Give the position of every leukocyte visible.
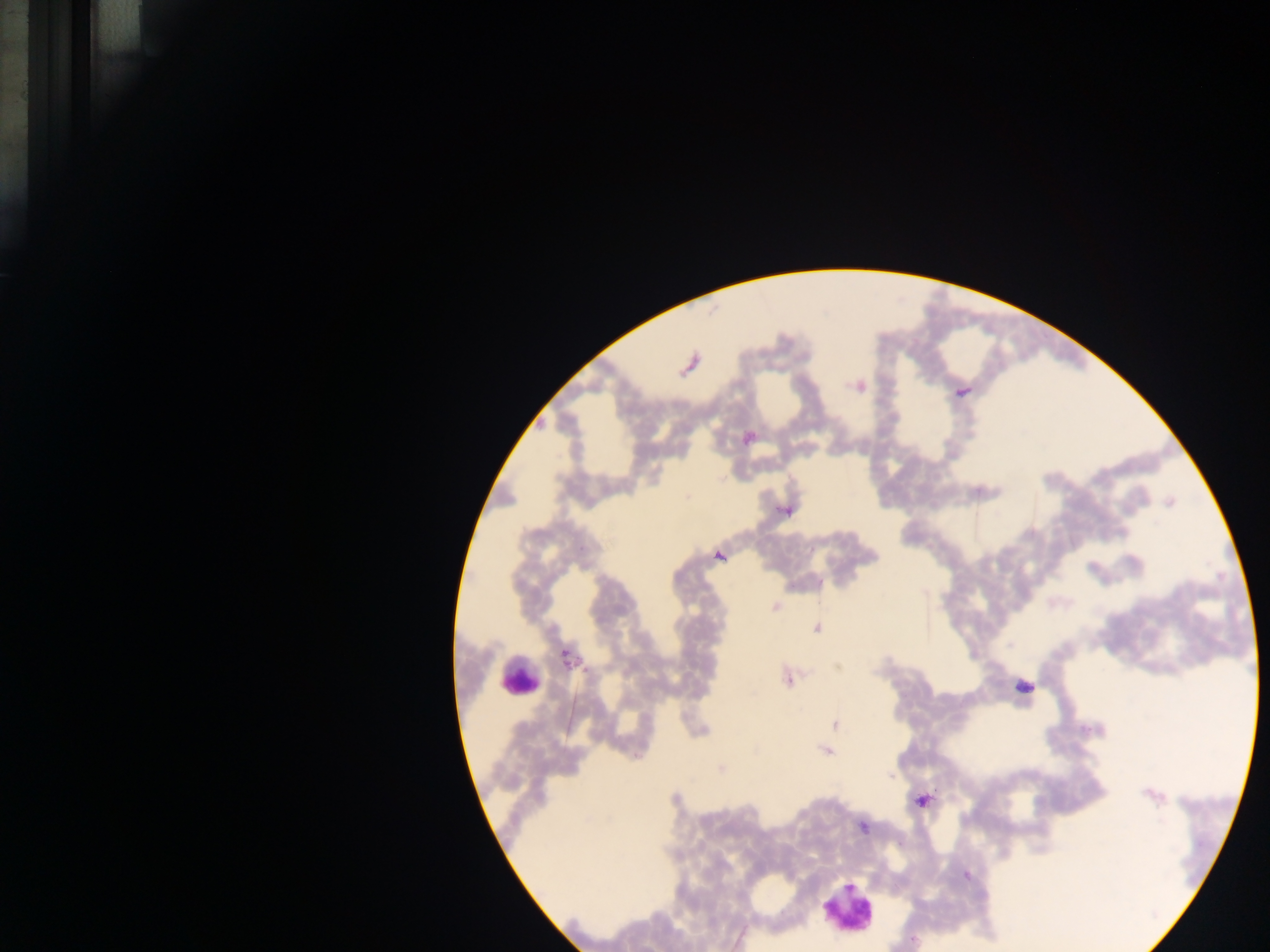

Approximate centers as x y in pixels.
Leukocytes: 518 676; 849 905.

Malaria parasite locations: 774 606; 816 628; 787 679; 835 724; 826 751; 720 768; 890 776; 920 801; 862 827. Mobile-phone photograph taken through the microscope. Image is 1270×952 pixels. Collected in Ghana. Thick blood smear. Single field of view.